Give the position of every malaria parasite.
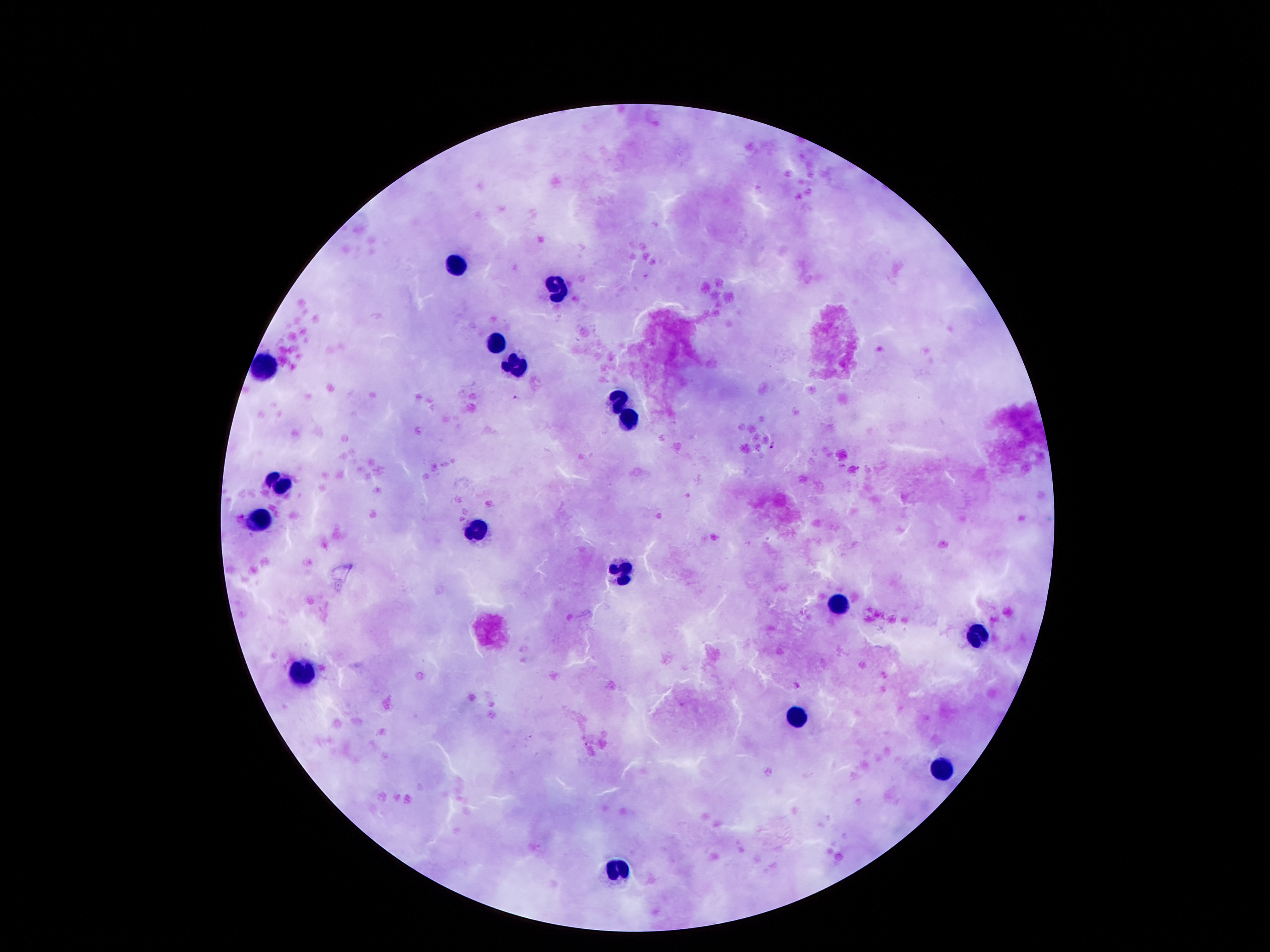
Approximate centers as {x, y} in pixels.
Malaria parasites: {514, 397}, {772, 445}.

Leukocyte locations: {459, 266}, {558, 288}, {495, 341}, {518, 364}, {266, 371}, {620, 399}, {627, 419}, {284, 482}, {259, 518}, {475, 529}, {620, 573}, {838, 604}, {979, 636}, {306, 673}, {801, 718}, {942, 770}, {618, 869}. Giemsa stain. 100x magnification. Image is 1270×952 pixels. Patient malaria status: positive for Plasmodium falciparum. Single field of view. Photographed through the microscope eyepiece with a smartphone camera. Thick peripheral-blood smear.